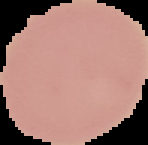

Summary:
  - Image type: segmented cell region with the area outside set to black
  - Image size: 148×145 pixels
  - Result: negative for Plasmodium parasites
  - Preparation: thin blood smear